Report the malaria status of this cell.
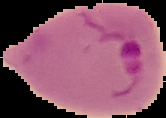

It is parasitized.

Image is 166×118 pixels. From a thin blood smear. Cell region segmented out of the field of view; the surrounding area is masked to black.